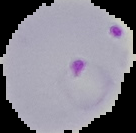 Image is 136×133 pixels. Segmented cell region on a black background. Result: Plasmodium parasites identified. From a thin blood smear.